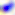

Micrograph. 400x magnification. Toxoplasma gondii is seen.